Describe the morphology of the erythrocytes.
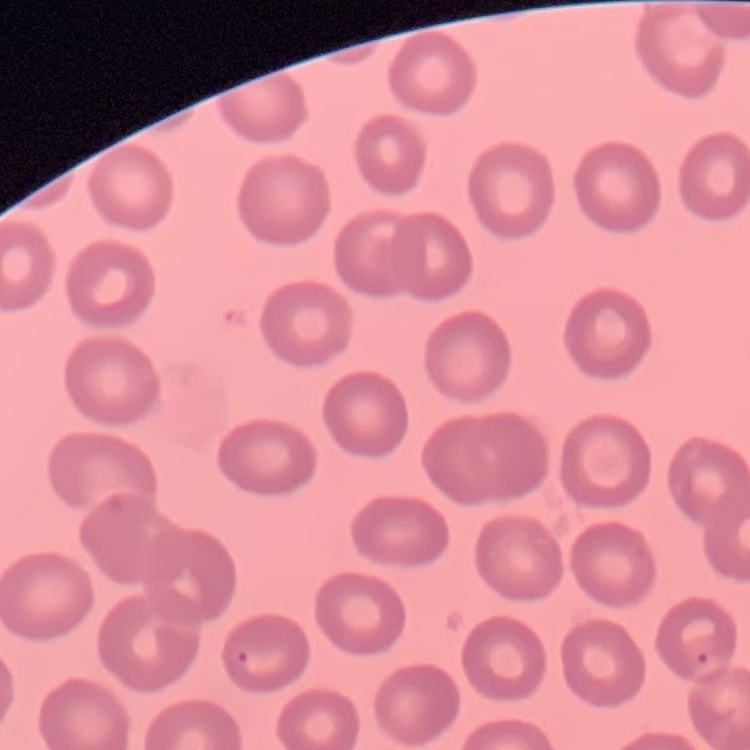
No rouleaux formation.

stain = Field's or Giemsa
image type = one tile cut from a larger photomicrograph
preparation = thin peripheral smear